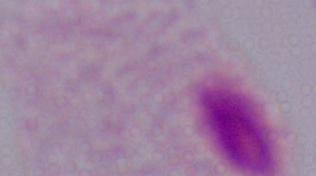 A trichomonad is seen. Photomicrograph. Captured at 1000x magnification.